Evaluate for Plasmodium parasites.
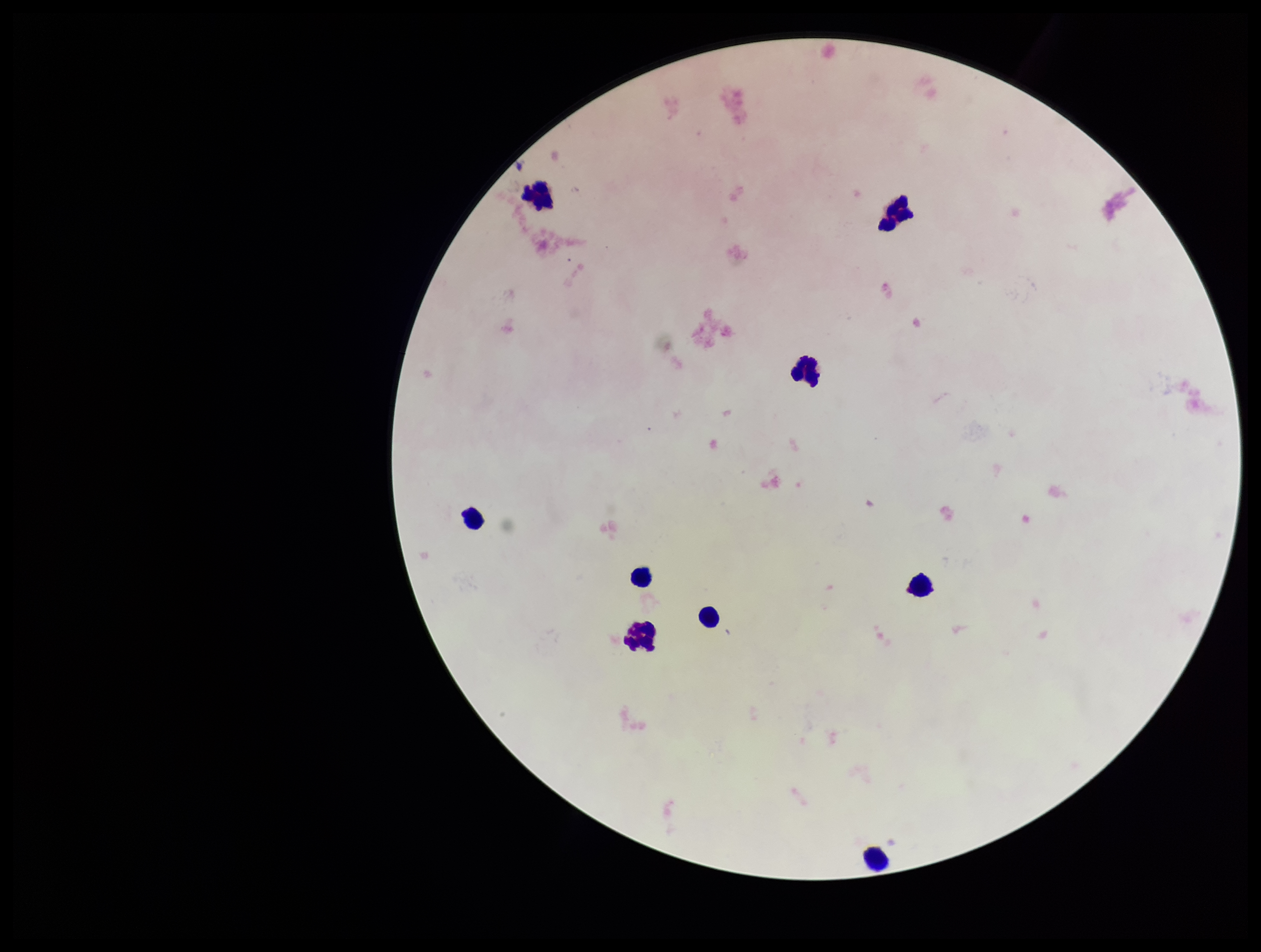

None detected.

{
  "stain": "Giemsa",
  "patient_malaria_status": "negative",
  "field_of_view": "single",
  "image_size": "1261×952 pixels",
  "leukocyte_count": 9,
  "capture": "smartphone photograph through the microscope eyepiece",
  "preparation": "thick smear",
  "parasite_count": 0
}